Report the malaria status of this cell.
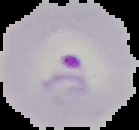

Parasitized.

image type = cell region segmented out of the field of view; surrounding area masked to black
preparation = thin blood film
image size = 139×130 pixels